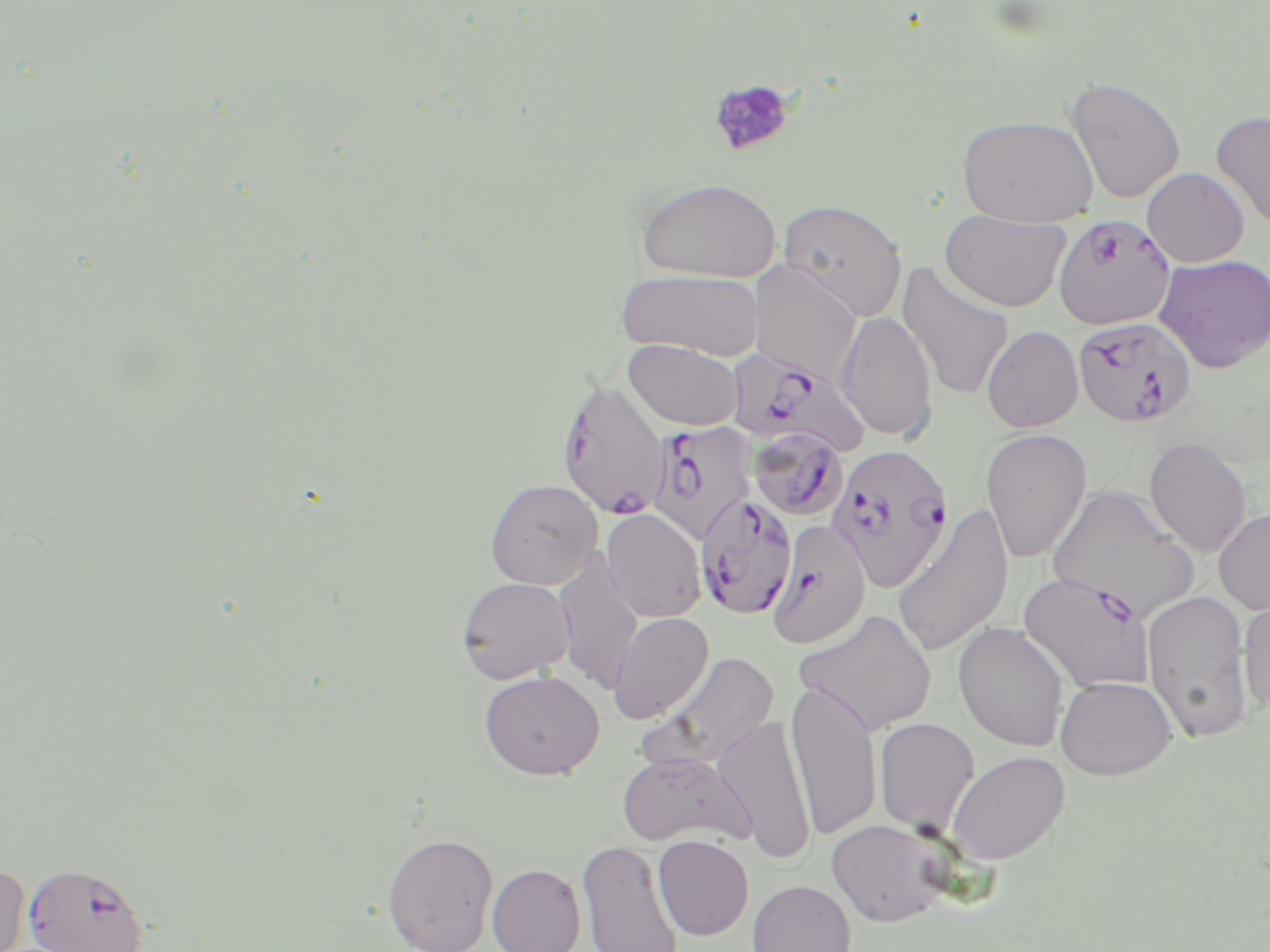

Summary:
  - Coordinate format: approximate bounding boxes as (x1,y1)-(x2,y2) corner pairs in pixels
  - Platelet locations: (707,77)-(798,157)
  - Uninfected red blood cell locations: (1064,76)-(1186,204), (1210,110)-(1270,233), (957,114)-(1098,227), (1142,167)-(1250,267), (635,177)-(782,283), (778,199)-(908,321), (939,208)-(1071,312), (1153,254)-(1270,373), (748,260)-(862,380), (896,261)-(1015,401), (615,267)-(766,360), (836,309)-(937,442), (982,325)-(1084,433), (623,339)-(744,431), (980,427)-(1092,564), (1144,435)-(1252,557), (484,478)-(603,589), (1047,484)-(1199,621), (891,505)-(1014,658), (1213,507)-(1270,615), (601,509)-(707,622), (553,549)-(644,695), (456,576)-(575,684), (1142,590)-(1255,744), (1238,595)-(1270,716), (793,608)-(937,735), (608,612)-(714,724), (952,621)-(1071,751), (653,651)-(780,768), (478,669)-(605,780), (1055,675)-(1177,780), (785,678)-(883,841), (712,712)-(817,865), (874,717)-(980,835), (616,749)-(754,849), (946,750)-(1070,865), (826,820)-(948,926), (382,832)-(499,952), (653,835)-(754,940), (576,839)-(684,952), (0,861)-(30,952), (487,863)-(586,952), (747,879)-(856,952)
  - Plasmodium falciparum-infected red blood cell locations: (1052,214)-(1176,331), (1072,316)-(1196,428), (728,347)-(869,456), (556,377)-(671,520), (646,421)-(754,544), (747,426)-(849,522), (826,443)-(956,592), (694,492)-(803,622), (766,519)-(871,649), (1019,570)-(1156,692), (23,861)-(149,951)
  - Slide-level diagnosis: Plasmodium falciparum
  - Magnification: 1000x
  - Field of view: one of a larger specimen
  - Modality: light microscopy
  - Preparation: thin blood smear
  - Image size: 1270×952 pixels
  - Stain: May-Grünwald-Giemsa